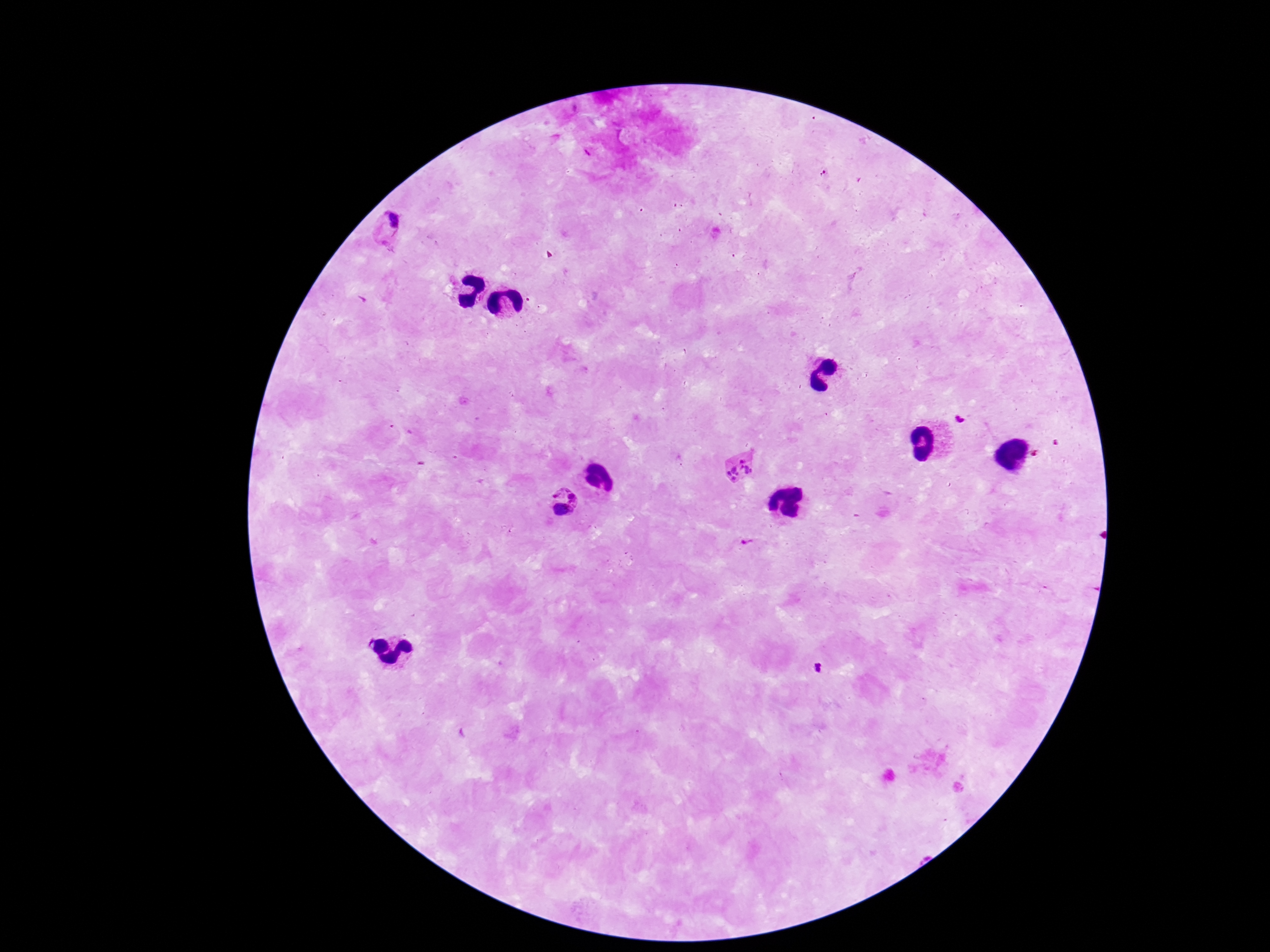
Approximate object centers, in pixels from the top-left corner.
Summary:
  - Plasmodium parasite locations: (x=385, y=228), (x=959, y=418), (x=1058, y=443), (x=1036, y=455), (x=741, y=467), (x=563, y=505), (x=746, y=543), (x=816, y=668)
  - Magnification: 100x
  - Preparation: thick blood film
  - Field of view: one from this slide
  - Capture: smartphone camera through the microscope eyepiece
  - Stain: Giemsa
  - Image size: 1270×952 pixels
  - Patient malaria status: infected